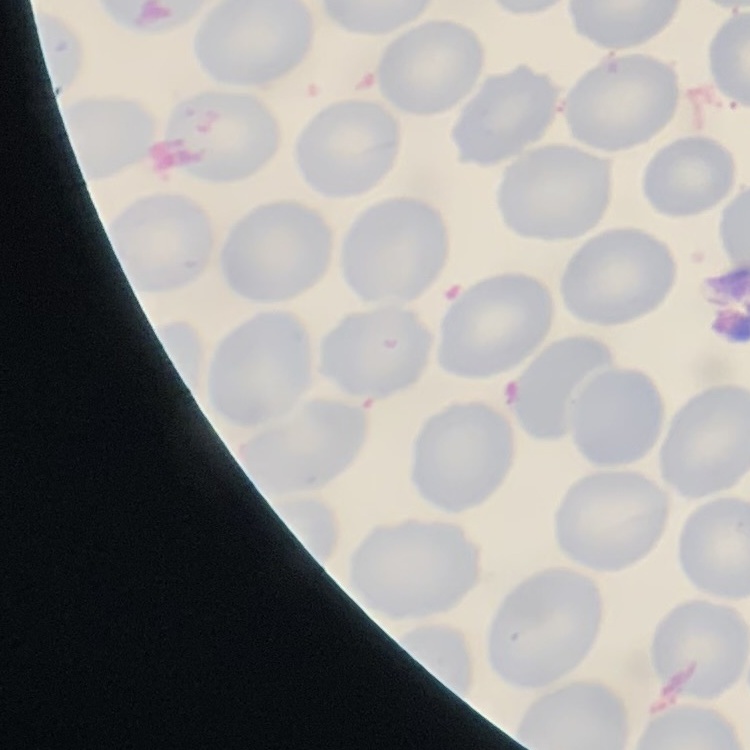

The erythrocytes show no rouleaux formation. Stained with either Field's or Giemsa. Thin peripheral smear. Square crop of a larger photomicrograph.